Identify the parasite.
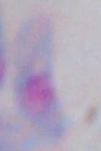
This is Toxoplasma gondii.

Micrograph. Captured at 1000x magnification.